Classify this cell by malaria status.
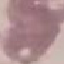
It is uninfected.

capture: smartphone through the microscope eyepiece
image_type: automatically extracted cell patch, resized to 64 × 64 pixels
preparation: thin smear
stain: Giemsa